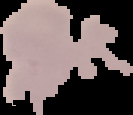
From a thin blood film. Image is 133×115 pixels. Result: no malaria parasites seen. Cell region segmented out of the field of view; the surrounding area is masked to black.